Give the position of every Plasmodium parasite visible.
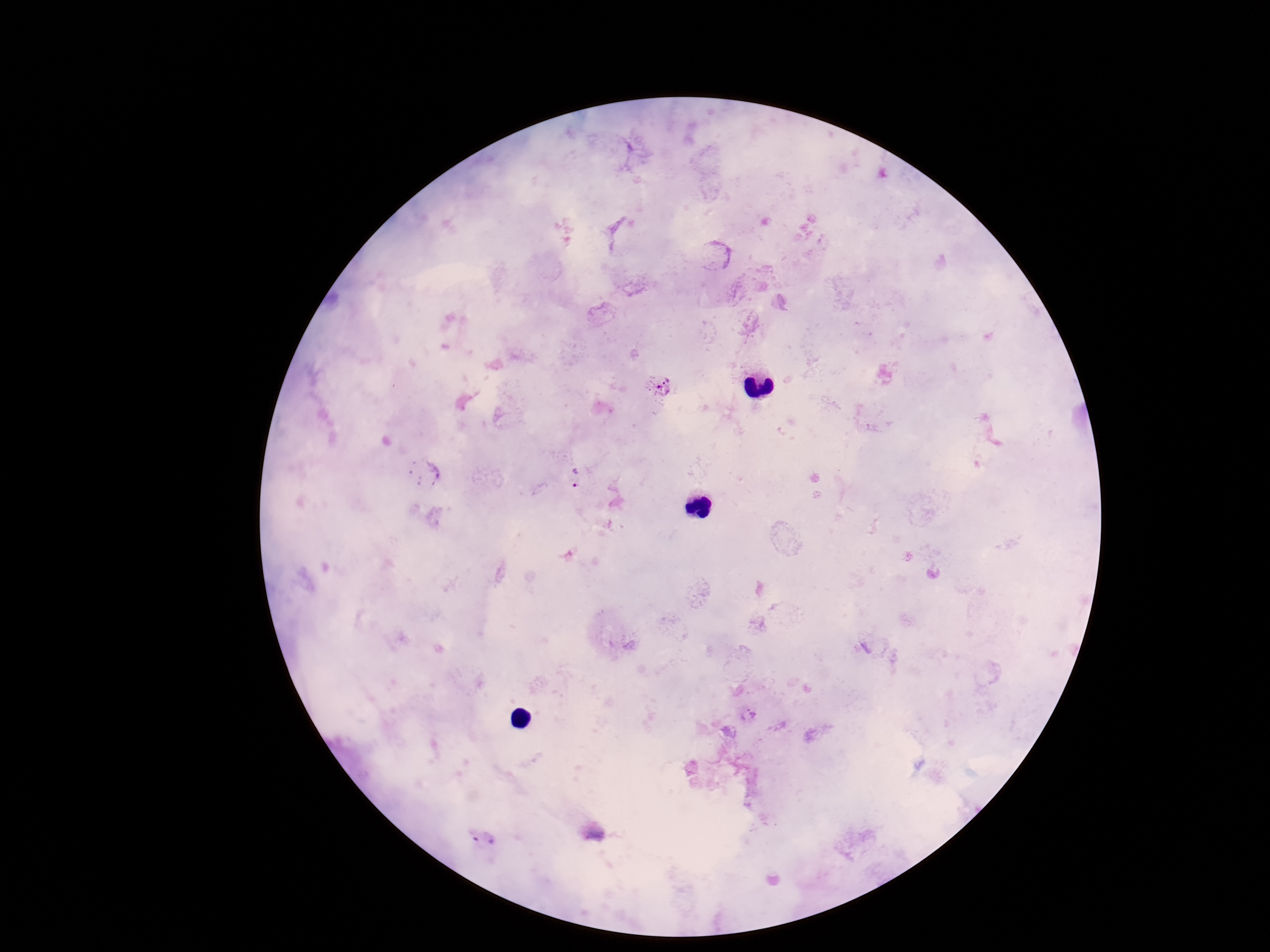
Approximate object centers, in pixels from the top-left corner.
Plasmodium parasites: (x=659, y=384), (x=575, y=477).

Thick blood smear. One field from this slide. Image is 1270×952 pixels. Patient malaria status: infected. 100x magnification. Giemsa stain. Smartphone photograph taken through the microscope eyepiece.